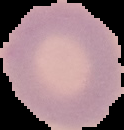

image type = cell region segmented out of the field of view; surrounding area masked to black
malaria status = uninfected
preparation = thin blood film
image size = 124×130 pixels